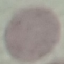

{
  "malaria_status": "uninfected",
  "stain": "Giemsa",
  "capture": "smartphone camera at the microscope eyepiece",
  "image_type": "cell patch, automatically extracted from a larger field of view and resized to 64 × 64 pixels",
  "preparation": "thin smear"
}